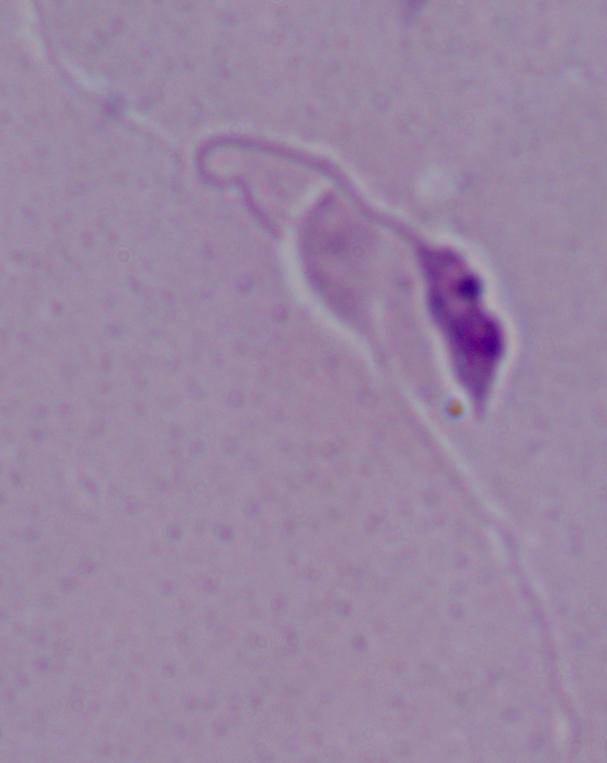
modality = photomicrograph
identification = Leishmania
magnification = 1000x